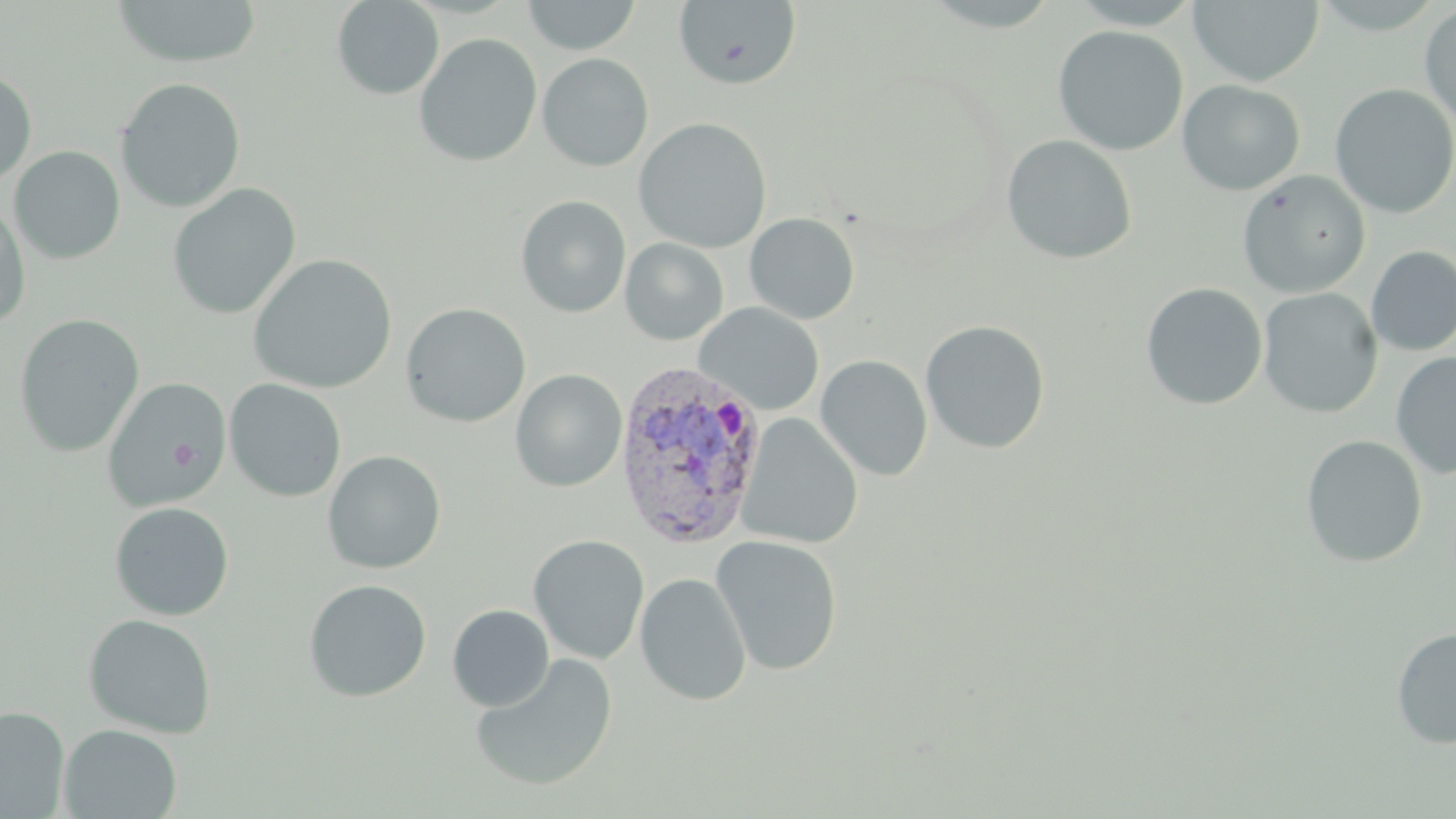

{
  "slide_level_diagnosis": "Plasmodium vivax",
  "platelet_locations": "approximate bounding boxes as named x1/y1/x2/y2 corners in pixels: (x1=170, y1=441, x2=198, y2=470)",
  "field_of_view": "one of a larger specimen",
  "magnification": "1000x",
  "modality": "optical microscopy",
  "plasmodium_vivax_infected_red_blood_cell_locations": "approximate bounding boxes as named x1/y1/x2/y2 corners in pixels: (x1=612, y1=360, x2=770, y2=550)",
  "preparation": "thin blood film",
  "stain": "May-Grünwald-Giemsa",
  "image_size": "1456×819 pixels",
  "uninfected_red_blood_cell_locations": "approximate bounding boxes as named x1/y1/x2/y2 corners in pixels: (x1=111, y1=0, x2=264, y2=69), (x1=331, y1=0, x2=444, y2=100), (x1=521, y1=0, x2=641, y2=55), (x1=1188, y1=0, x2=1324, y2=87), (x1=672, y1=1, x2=803, y2=91), (x1=1419, y1=4, x2=1456, y2=129), (x1=1052, y1=25, x2=1189, y2=156), (x1=414, y1=33, x2=542, y2=167), (x1=536, y1=53, x2=653, y2=171), (x1=0, y1=69, x2=37, y2=185), (x1=115, y1=77, x2=246, y2=213), (x1=1177, y1=79, x2=1304, y2=196), (x1=1329, y1=83, x2=1456, y2=219), (x1=634, y1=117, x2=772, y2=253), (x1=1001, y1=134, x2=1137, y2=265), (x1=9, y1=146, x2=125, y2=264), (x1=1237, y1=170, x2=1371, y2=298), (x1=166, y1=183, x2=302, y2=320), (x1=0, y1=195, x2=32, y2=329), (x1=515, y1=195, x2=631, y2=318), (x1=744, y1=213, x2=860, y2=325), (x1=620, y1=237, x2=729, y2=345), (x1=1366, y1=245, x2=1456, y2=356), (x1=248, y1=253, x2=398, y2=394), (x1=1140, y1=282, x2=1268, y2=411), (x1=1258, y1=287, x2=1382, y2=418), (x1=400, y1=302, x2=531, y2=427), (x1=694, y1=302, x2=825, y2=415), (x1=14, y1=314, x2=144, y2=457), (x1=919, y1=320, x2=1051, y2=454), (x1=1390, y1=350, x2=1456, y2=481), (x1=815, y1=355, x2=933, y2=481), (x1=510, y1=369, x2=627, y2=492), (x1=101, y1=376, x2=230, y2=511), (x1=225, y1=378, x2=347, y2=502), (x1=739, y1=413, x2=862, y2=549), (x1=1300, y1=435, x2=1428, y2=568), (x1=322, y1=450, x2=446, y2=574), (x1=109, y1=501, x2=234, y2=621), (x1=528, y1=534, x2=650, y2=664), (x1=710, y1=534, x2=843, y2=676), (x1=635, y1=572, x2=751, y2=706), (x1=303, y1=579, x2=432, y2=703), (x1=447, y1=604, x2=554, y2=711), (x1=82, y1=613, x2=216, y2=738), (x1=1391, y1=626, x2=1456, y2=750), (x1=469, y1=653, x2=618, y2=792), (x1=0, y1=706, x2=69, y2=817), (x1=59, y1=723, x2=182, y2=818)"
}